Locate every blood parasite and identify its species.
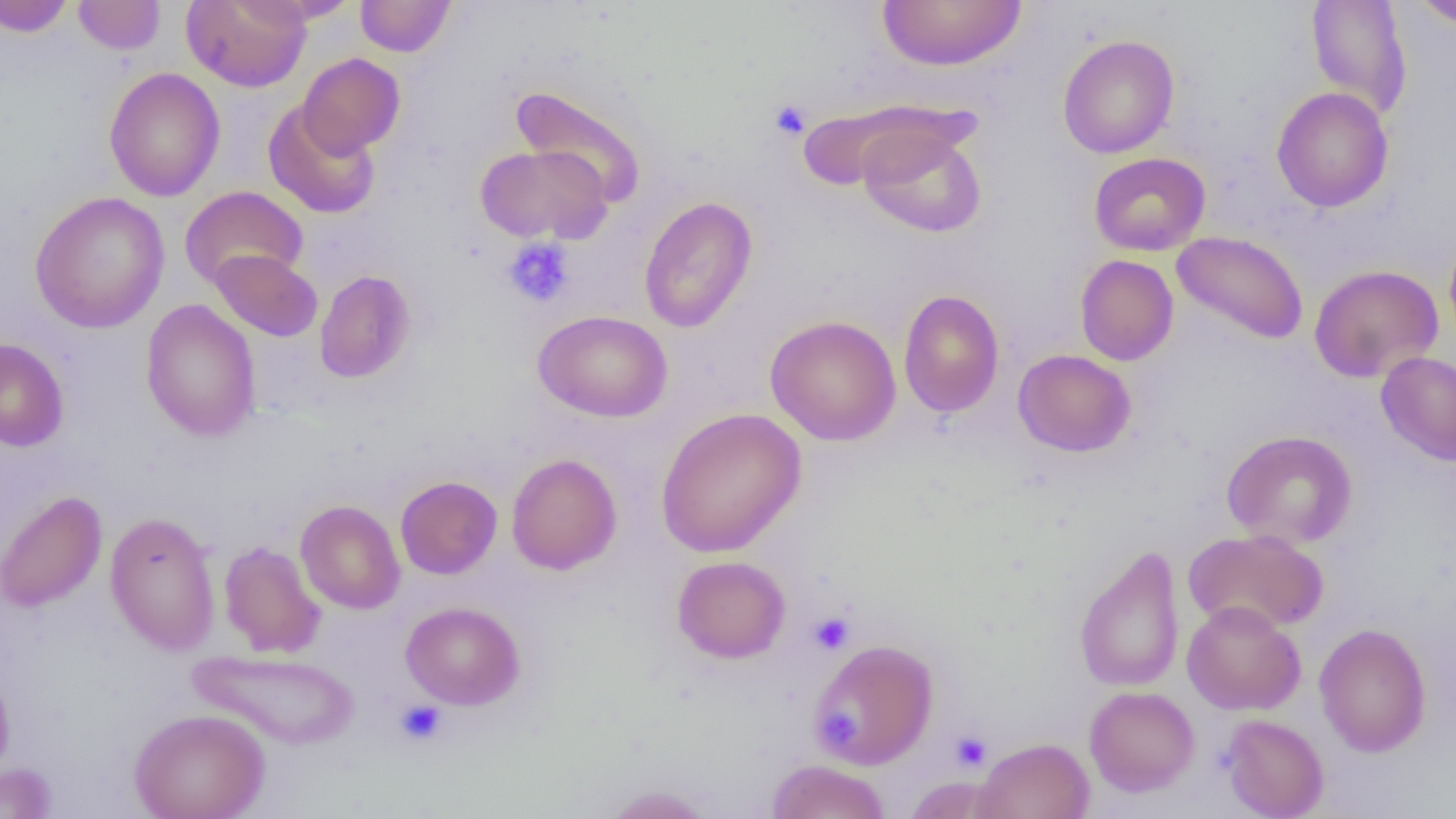
No blood parasites seen.

slide-level diagnosis = no evidence of blood parasites
field of view = single
preparation = thin blood smear
modality = light microscopy
image size = 1456×819 pixels
platelet locations = approximate bounding boxes as named x1/y1/x2/y2 corners in pixels: (x1=769, y1=99, x2=811, y2=140), (x1=501, y1=238, x2=575, y2=309), (x1=809, y1=612, x2=854, y2=654), (x1=395, y1=700, x2=446, y2=745), (x1=823, y1=707, x2=860, y2=743), (x1=951, y1=732, x2=991, y2=771)
magnification = 1000x
uninfected red blood cell locations = approximate bounding boxes as named x1/y1/x2/y2 corners in pixels: (x1=73, y1=0, x2=165, y2=55), (x1=181, y1=0, x2=311, y2=92), (x1=241, y1=0, x2=362, y2=25), (x1=356, y1=0, x2=455, y2=57), (x1=877, y1=0, x2=1026, y2=72), (x1=1412, y1=0, x2=1456, y2=28), (x1=0, y1=1, x2=74, y2=36), (x1=1306, y1=1, x2=1413, y2=121), (x1=1057, y1=34, x2=1180, y2=159), (x1=298, y1=53, x2=404, y2=156), (x1=104, y1=67, x2=226, y2=202), (x1=511, y1=86, x2=647, y2=206), (x1=1271, y1=86, x2=1394, y2=212), (x1=263, y1=101, x2=381, y2=219), (x1=858, y1=124, x2=987, y2=238), (x1=475, y1=144, x2=611, y2=244), (x1=1088, y1=152, x2=1210, y2=256), (x1=180, y1=186, x2=308, y2=290), (x1=30, y1=191, x2=170, y2=334), (x1=639, y1=196, x2=758, y2=334), (x1=1443, y1=228, x2=1456, y2=349), (x1=1171, y1=231, x2=1309, y2=344), (x1=208, y1=249, x2=323, y2=342), (x1=1075, y1=254, x2=1179, y2=366), (x1=1309, y1=264, x2=1444, y2=383), (x1=314, y1=270, x2=416, y2=384), (x1=898, y1=289, x2=1005, y2=418), (x1=140, y1=299, x2=261, y2=442), (x1=533, y1=309, x2=672, y2=423), (x1=765, y1=315, x2=902, y2=446), (x1=0, y1=337, x2=69, y2=452), (x1=1013, y1=349, x2=1136, y2=457), (x1=1376, y1=351, x2=1456, y2=467), (x1=655, y1=407, x2=806, y2=558), (x1=1221, y1=430, x2=1358, y2=549), (x1=506, y1=453, x2=622, y2=575), (x1=395, y1=476, x2=502, y2=579), (x1=0, y1=490, x2=107, y2=612), (x1=295, y1=500, x2=405, y2=614), (x1=104, y1=511, x2=222, y2=656), (x1=1183, y1=528, x2=1329, y2=635), (x1=219, y1=541, x2=326, y2=657), (x1=1073, y1=543, x2=1186, y2=693), (x1=671, y1=555, x2=791, y2=663), (x1=1181, y1=600, x2=1306, y2=715), (x1=400, y1=601, x2=525, y2=710), (x1=1314, y1=622, x2=1432, y2=757), (x1=809, y1=639, x2=938, y2=769), (x1=188, y1=648, x2=362, y2=750), (x1=0, y1=666, x2=15, y2=782), (x1=1084, y1=686, x2=1200, y2=797), (x1=129, y1=708, x2=270, y2=819), (x1=1220, y1=713, x2=1329, y2=819), (x1=973, y1=737, x2=1094, y2=819), (x1=766, y1=759, x2=891, y2=819), (x1=0, y1=763, x2=58, y2=819), (x1=902, y1=775, x2=1011, y2=818), (x1=600, y1=784, x2=715, y2=818)